Outline platelets.
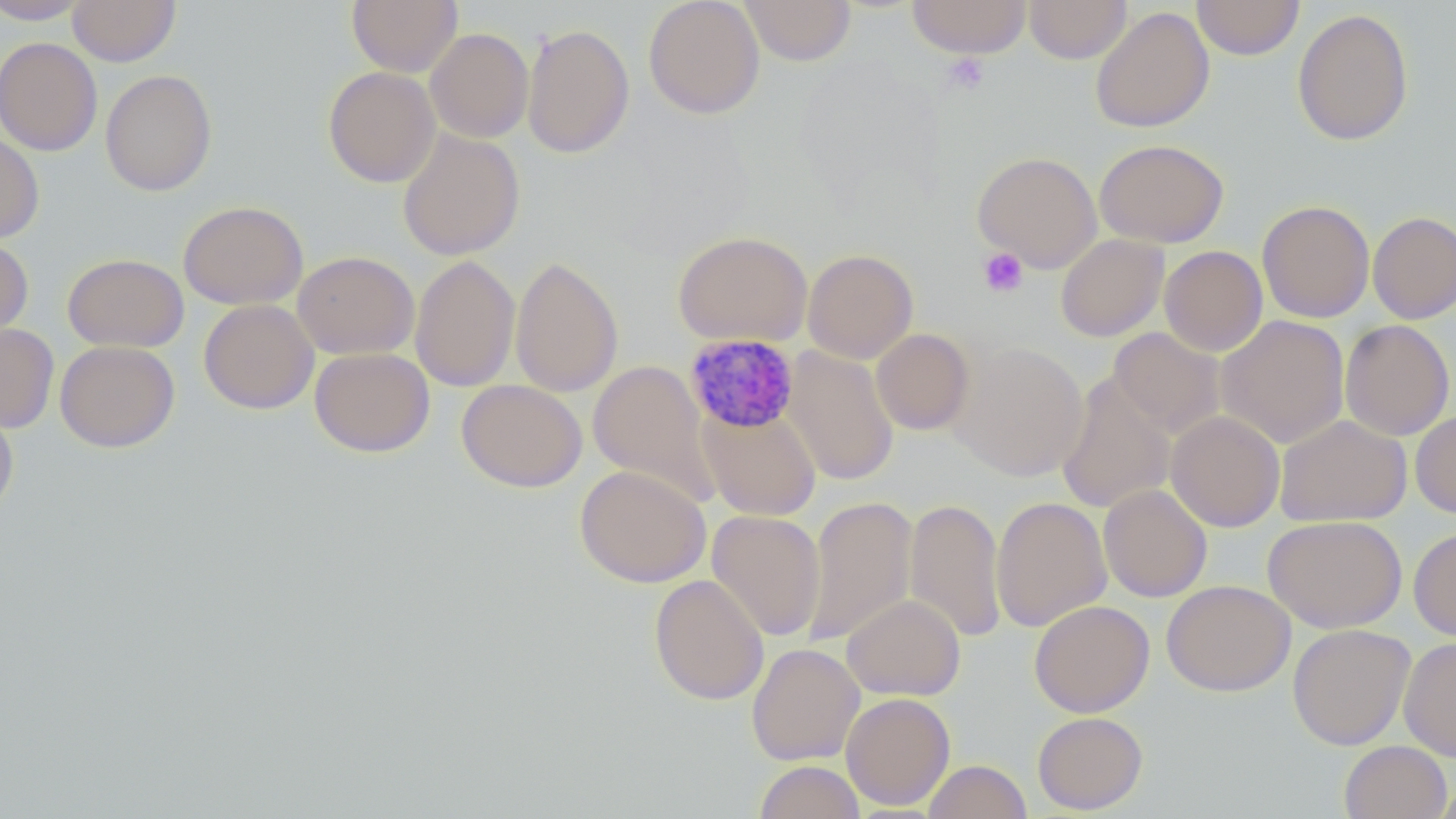
Approximate bounding boxes as (x1,y1)-(x2,y2) corner pairs in pixels.
Platelets: (942,54)-(990,94), (978,247)-(1028,298).

Summary:
  - Uninfected red blood cell locations: (67,0)-(180,66), (347,0)-(462,76), (644,0)-(765,119), (739,0)-(856,66), (907,0)-(1032,58), (1024,0)-(1132,64), (1192,0)-(1304,60), (0,1)-(92,24), (1090,6)-(1215,133), (1292,8)-(1414,146), (522,23)-(634,159), (425,28)-(534,143), (0,37)-(102,156), (322,66)-(441,187), (100,69)-(217,196), (397,129)-(526,261), (0,131)-(44,243), (1094,138)-(1230,248), (971,151)-(1103,273), (178,200)-(308,310), (1257,200)-(1375,323), (1367,211)-(1456,324), (673,230)-(813,347), (1055,234)-(1169,342), (0,235)-(34,340), (1159,245)-(1267,356), (802,248)-(919,364), (292,251)-(420,359), (62,253)-(189,352), (410,254)-(520,392), (510,255)-(624,398), (198,299)-(319,415), (1216,315)-(1350,448), (1340,319)-(1454,440), (0,323)-(59,433), (871,328)-(975,435), (1109,328)-(1226,438), (55,340)-(180,452), (948,341)-(1088,481), (782,346)-(899,486), (309,347)-(435,458), (587,360)-(719,504), (1056,372)-(1176,514), (456,379)-(588,493), (0,399)-(19,520), (698,404)-(821,520), (1165,411)-(1285,532), (1410,411)-(1456,518), (1275,414)-(1412,527), (574,465)-(711,588), (1098,484)-(1212,602), (802,495)-(918,647), (991,496)-(1112,632), (904,497)-(1007,643), (707,509)-(826,642), (1263,515)-(1408,633), (1408,527)-(1456,641), (649,574)-(769,705), (1161,579)-(1295,697), (842,594)-(966,701), (1029,599)-(1155,717), (1287,623)-(1415,750), (1399,636)-(1456,761), (746,643)-(865,766), (841,692)-(956,810), (1032,711)-(1148,814), (1338,740)-(1452,819), (922,759)-(1031,819), (754,760)-(865,819), (1432,776)-(1456,818)
  - Plasmodium malariae-infected red blood cell locations: (684,332)-(800,434)
  - Slide-level diagnosis: Plasmodium malariae
  - Field of view: single
  - Modality: optical microscopy
  - Magnification: 1000x
  - Stain: May-Grünwald-Giemsa
  - Image size: 1456×819 pixels
  - Preparation: thin blood film